Assess this cell for malaria.
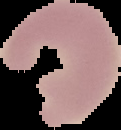
It is uninfected.

Image is 121×130 pixels. From a thin blood film. The area outside the segmented cell region is set to black.